Assess for Plasmodium parasites.
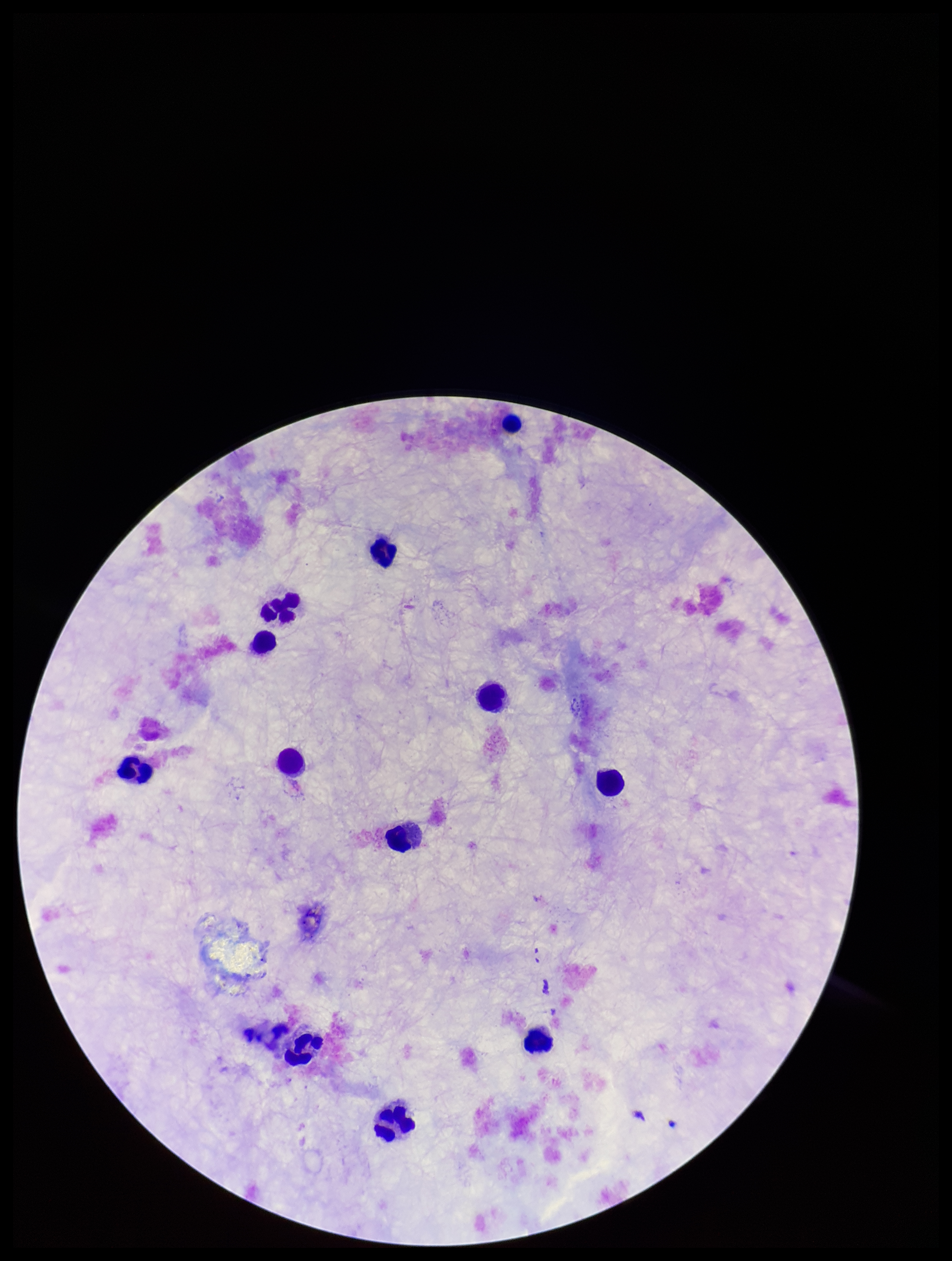

None seen.

parasite count = 0
image size = 952×1261 pixels
stain = Giemsa
leukocyte count = 12
preparation = thick blood smear
patient malaria status = negative
field of view = one from this slide
capture = smartphone photograph through the microscope eyepiece